Identify the blood parasite species.
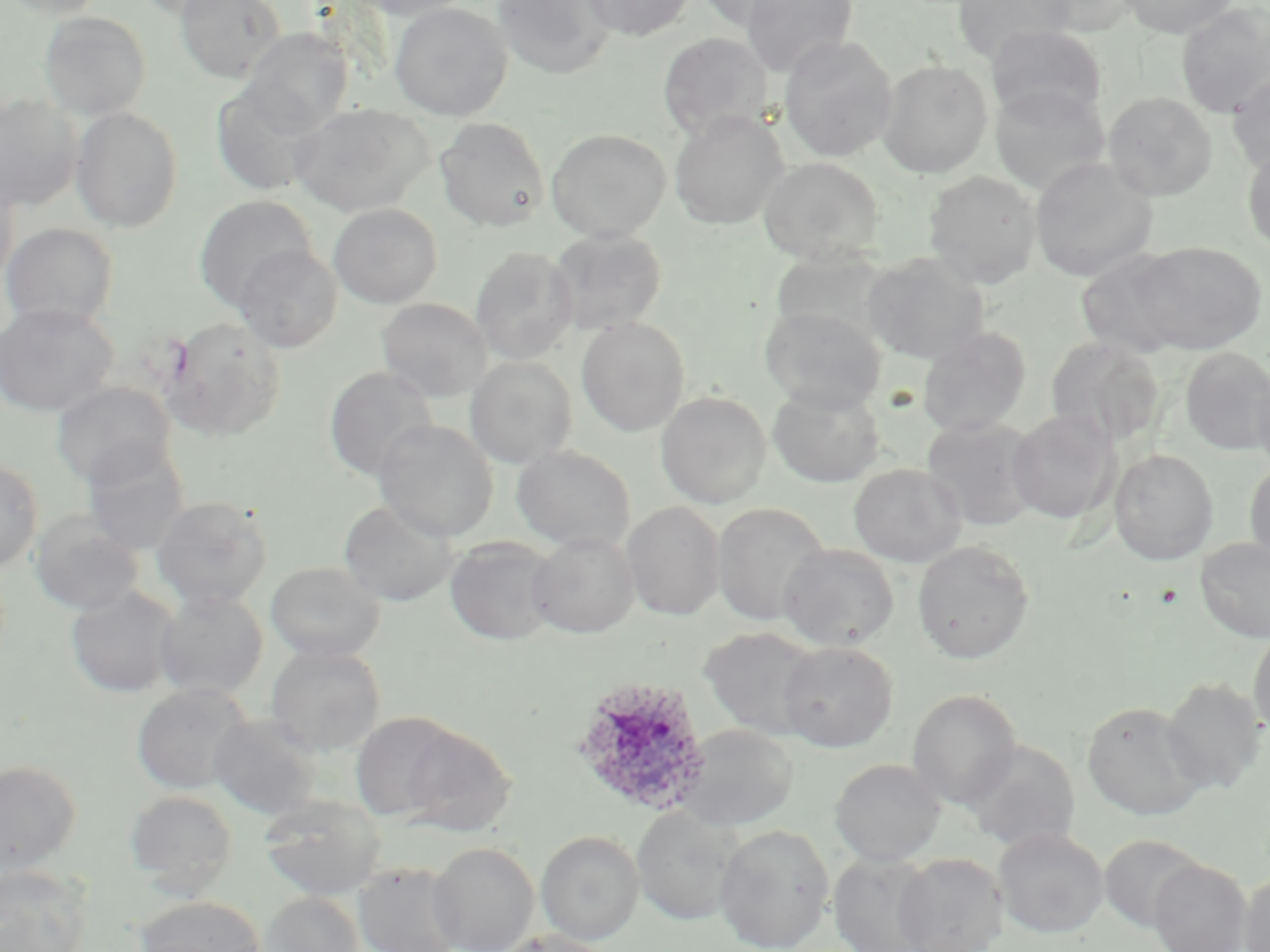
Plasmodium ovale.

Approximate bounding boxes as (x1, y1, x2, y2) in pixels. Uninfected red blood cell locations: (3, 0, 107, 18), (133, 0, 245, 20), (175, 0, 287, 83), (344, 0, 473, 21), (492, 0, 616, 79), (584, 0, 695, 41), (695, 0, 804, 29), (740, 0, 857, 77), (950, 0, 1075, 64), (1032, 0, 1142, 34), (1120, 0, 1238, 38), (389, 2, 512, 121), (1176, 3, 1270, 117), (40, 12, 151, 119), (985, 25, 1107, 125), (241, 29, 353, 133), (657, 32, 773, 142), (779, 35, 897, 162), (877, 59, 993, 177), (1228, 72, 1270, 176), (211, 81, 329, 196), (990, 84, 1111, 195), (1103, 91, 1217, 201), (0, 93, 83, 211), (290, 103, 432, 217), (70, 107, 184, 232), (669, 111, 788, 230), (434, 117, 550, 231), (546, 128, 671, 242), (1242, 144, 1270, 254), (759, 157, 884, 264), (1029, 157, 1158, 283), (923, 170, 1041, 288), (0, 172, 19, 290), (193, 195, 318, 312), (328, 203, 443, 308), (1, 222, 119, 328), (547, 228, 668, 335), (1129, 241, 1267, 355), (234, 244, 342, 352), (470, 246, 578, 365), (1075, 251, 1189, 359), (862, 252, 989, 364), (376, 298, 492, 402), (0, 302, 118, 417), (759, 306, 886, 413), (161, 316, 286, 440), (576, 318, 690, 436), (917, 327, 1032, 437), (1046, 336, 1164, 447), (1179, 346, 1270, 454), (464, 356, 577, 469), (324, 366, 437, 482), (1250, 367, 1270, 478), (51, 381, 176, 486), (767, 384, 885, 487), (655, 391, 771, 508), (1007, 409, 1120, 524), (921, 416, 1041, 531), (374, 420, 498, 541), (81, 440, 191, 553), (511, 445, 636, 551), (1110, 449, 1218, 564), (0, 459, 42, 572), (1244, 461, 1270, 569), (848, 464, 967, 566), (150, 495, 274, 610), (338, 499, 458, 605), (623, 501, 725, 620), (711, 502, 830, 626), (29, 511, 144, 616), (528, 532, 639, 638), (444, 537, 561, 646), (1195, 537, 1270, 643), (912, 540, 1035, 664), (779, 543, 899, 650), (265, 561, 385, 662), (65, 585, 181, 698), (154, 589, 268, 700), (1248, 625, 1270, 739), (700, 626, 823, 739), (778, 641, 898, 751), (266, 643, 386, 756), (1162, 677, 1267, 793), (131, 683, 253, 795), (907, 689, 1023, 809), (1081, 700, 1208, 820), (350, 712, 463, 823), (209, 714, 323, 819), (399, 723, 517, 837), (679, 723, 798, 831), (962, 739, 1081, 852), (829, 758, 946, 865), (0, 761, 81, 875), (125, 790, 237, 895), (258, 793, 387, 900), (631, 804, 742, 926), (714, 824, 834, 951), (993, 827, 1109, 938), (536, 830, 644, 944), (1099, 834, 1208, 932), (428, 842, 539, 952), (828, 851, 942, 951), (892, 852, 1010, 952), (1148, 858, 1253, 952), (352, 862, 463, 952), (0, 865, 92, 952), (1240, 868, 1270, 952), (258, 892, 365, 952), (137, 895, 266, 952), (495, 930, 620, 952). Plasmodium ovale-infected red blood cell locations: (572, 676, 712, 818). Image is 1270×952 pixels. Thin blood smear. May-Grünwald-Giemsa-stained preparation. Light microscopy. Captured at 1000x magnification. One field of a larger specimen.